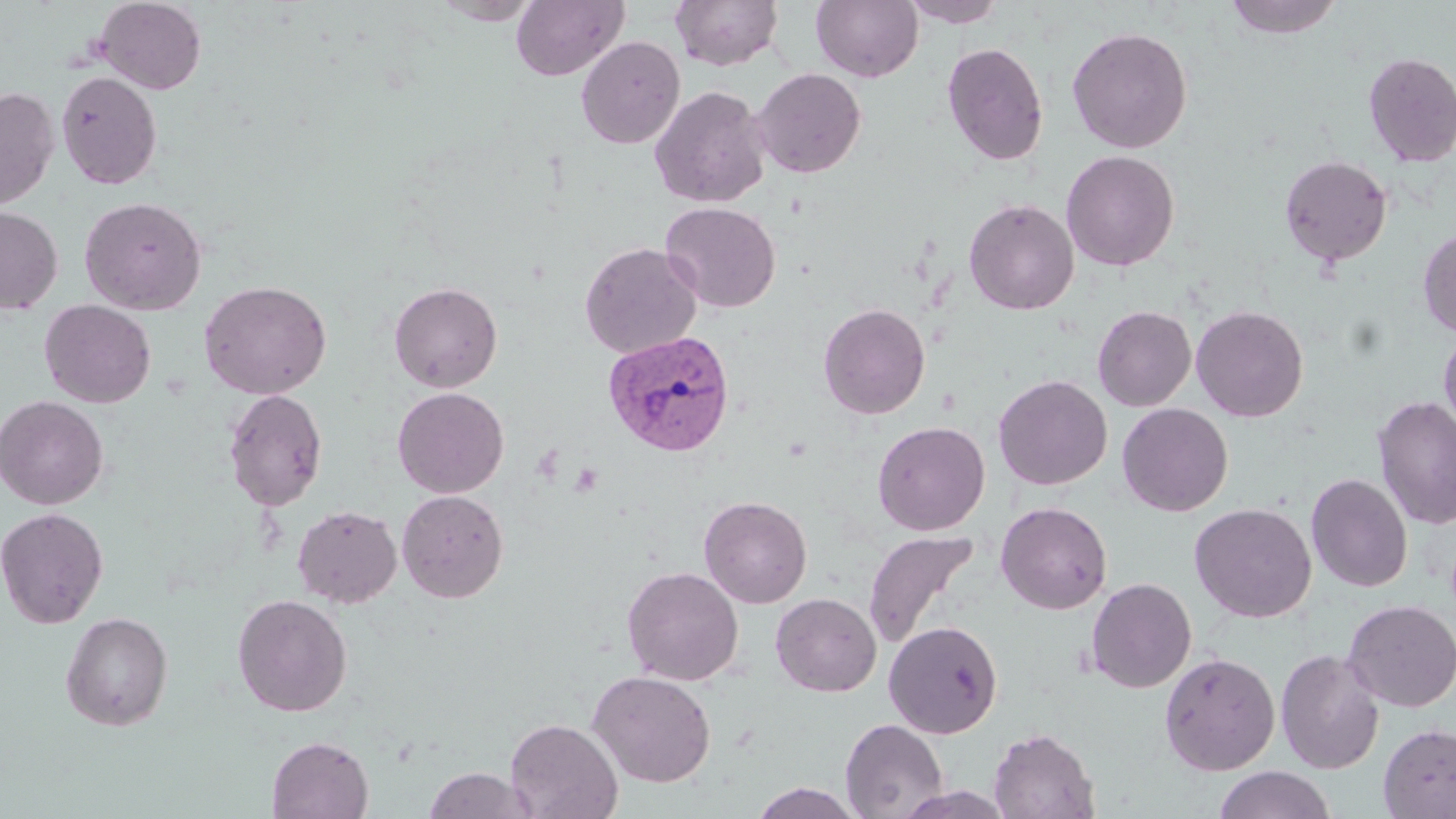

Approximate bounding boxes as (x1, y1, x2, y2) in pixels. Uninfected red blood cell locations: (95, 0, 206, 94), (670, 0, 783, 71), (811, 0, 923, 83), (1223, 0, 1343, 39), (431, 1, 543, 25), (510, 1, 629, 82), (899, 1, 1008, 27), (1067, 26, 1192, 154), (576, 36, 685, 149), (941, 42, 1048, 166), (1362, 52, 1456, 168), (751, 67, 867, 178), (56, 70, 162, 189), (649, 85, 770, 208), (0, 86, 59, 211), (1061, 150, 1180, 271), (1279, 154, 1393, 267), (80, 196, 207, 315), (964, 198, 1080, 315), (660, 202, 781, 313), (0, 206, 63, 314), (1418, 228, 1456, 338), (579, 242, 701, 358), (199, 280, 332, 399), (389, 281, 503, 392), (39, 300, 156, 408), (818, 303, 930, 419), (1191, 305, 1309, 422), (1092, 306, 1196, 411), (1439, 325, 1456, 440), (993, 375, 1112, 490), (392, 387, 509, 498), (223, 388, 328, 511), (0, 395, 108, 510), (1372, 395, 1456, 530), (1117, 403, 1233, 516), (872, 421, 990, 535), (1306, 472, 1413, 592), (396, 489, 509, 603), (699, 495, 812, 608), (995, 501, 1113, 614), (1189, 503, 1316, 622), (292, 505, 402, 607), (0, 507, 109, 628), (862, 529, 979, 648), (622, 566, 744, 686), (1085, 577, 1197, 693), (771, 593, 881, 696), (232, 594, 352, 717), (1342, 599, 1456, 712), (60, 611, 173, 730), (884, 621, 1003, 738), (1275, 648, 1385, 774), (1158, 651, 1280, 775), (588, 670, 717, 787), (505, 718, 623, 819), (840, 718, 948, 818), (1378, 723, 1456, 818), (988, 727, 1100, 818), (267, 736, 374, 819), (1214, 766, 1336, 818), (423, 767, 537, 819), (748, 783, 865, 818), (898, 787, 1016, 819). Plasmodium vivax-infected red blood cell locations: (602, 330, 736, 457). Slide-level diagnosis: Plasmodium vivax. Image is 1456×819 pixels. Optical microscopy. May-Grünwald-Giemsa-stained preparation. Thin blood film. Captured at 1000x magnification. One field of a larger specimen.